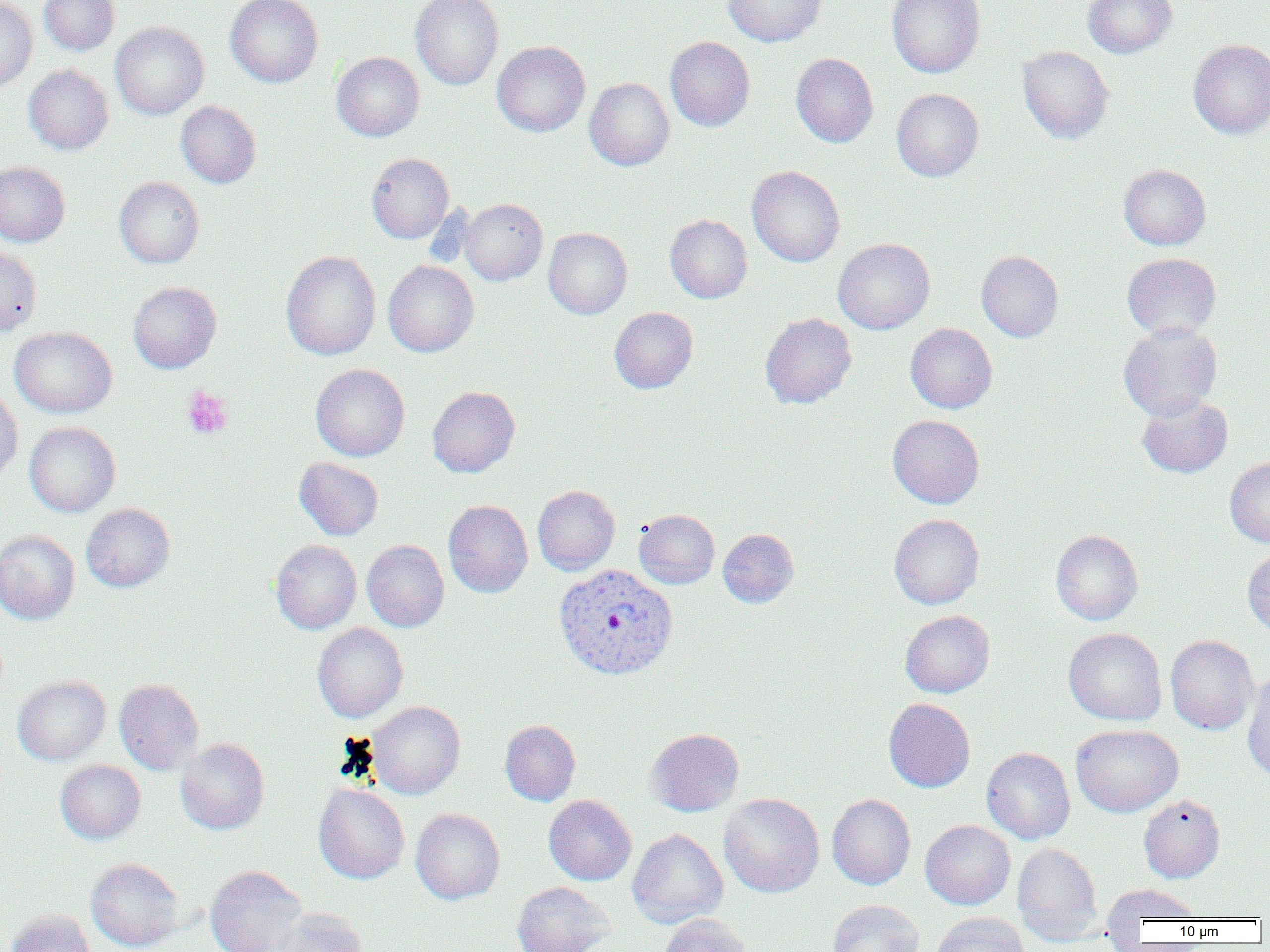

Approximate bounding boxes as (x1,y1)-(x2,y2) corner pairs in pixels. Platelet locations: (182,388)-(234,440). Uninfected red blood cell locations: (38,0)-(119,55), (225,0)-(323,88), (410,0)-(503,91), (723,0)-(826,47), (886,0)-(985,79), (1083,0)-(1177,58), (0,1)-(38,92), (110,22)-(209,120), (665,36)-(755,132), (1188,39)-(1270,139), (492,41)-(590,137), (1018,45)-(1114,144), (331,52)-(424,142), (791,53)-(878,148), (23,65)-(113,155), (584,78)-(674,171), (891,88)-(984,182), (176,101)-(261,188), (366,152)-(454,243), (0,161)-(70,247), (1118,164)-(1211,250), (746,165)-(845,267), (114,177)-(205,269), (459,198)-(547,285), (665,214)-(752,303), (543,228)-(632,319), (833,238)-(935,334), (0,244)-(42,337), (280,250)-(381,360), (976,250)-(1063,342), (1122,252)-(1221,340), (383,260)-(479,357), (128,281)-(221,374), (609,307)-(697,394), (759,313)-(857,409), (1118,322)-(1223,420), (905,323)-(997,413), (9,327)-(117,419), (310,364)-(410,461), (0,384)-(23,482), (427,386)-(520,477), (1136,393)-(1233,478), (887,415)-(985,508), (24,422)-(120,517), (294,457)-(383,540), (1225,457)-(1270,548), (532,485)-(620,575), (443,500)-(533,598), (80,502)-(175,593), (633,509)-(719,589), (889,513)-(984,609), (718,529)-(799,608), (0,530)-(80,625), (1051,530)-(1143,625), (270,540)-(362,634), (361,540)-(449,632), (1242,546)-(1270,637), (900,610)-(995,698), (312,623)-(408,723), (1063,627)-(1167,726), (1165,635)-(1258,735), (1242,672)-(1270,782), (13,675)-(111,765), (114,679)-(204,775), (884,698)-(975,793), (367,701)-(465,799), (500,720)-(581,805), (1071,724)-(1183,817), (644,728)-(744,817), (175,738)-(269,835), (981,747)-(1075,845), (55,760)-(146,844), (313,784)-(409,884), (719,793)-(824,898), (827,794)-(915,889), (1139,794)-(1225,883), (543,795)-(636,885), (410,808)-(504,904), (920,820)-(1015,910), (627,829)-(728,928), (1012,843)-(1103,946), (85,858)-(185,952), (205,865)-(307,952), (511,881)-(614,952), (1102,883)-(1202,929), (827,900)-(924,952), (274,907)-(367,952), (4,910)-(98,952), (930,912)-(1029,952), (659,914)-(751,952). Plasmodium vivax-infected red blood cell locations: (553,563)-(678,680). Slide-level diagnosis: Plasmodium vivax. One field of a larger specimen. Light microscopy. Image is 1270×952 pixels. Captured at 1000x magnification. Thin blood smear.